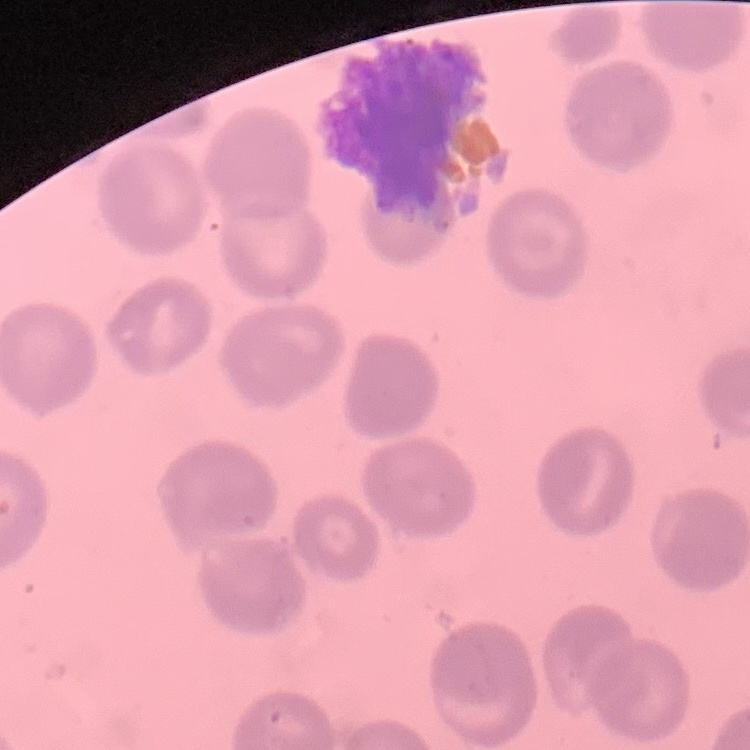

Summary:
  - Red blood cell morphology: no rouleaux formation
  - Stain: Field's or Giemsa
  - Preparation: thin blood smear
  - Image type: square crop of a larger photomicrograph